Identify the parasite.
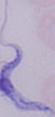

This is a trypanosome.

1000x magnification. Micrograph.